Mark where leukocytes are.
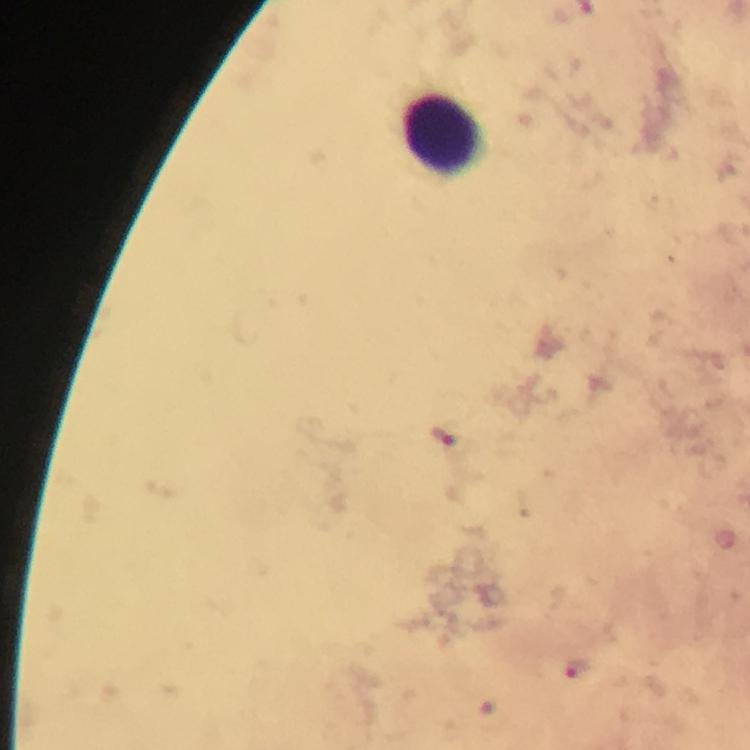
Approximate centers as {x, y} in pixels.
Leukocytes: {440, 136}.

Summary:
  - Plasmodium parasite locations: {443, 435}, {577, 668}
  - Immersion oil: used
  - Cropped from: one field of view
  - Stain: Giemsa
  - Capture: smartphone photograph through a microscope
  - Preparation: thick smear
  - Context: from a diagnostic examination for malaria
  - Magnification: 100x
  - Image size: 750×750 pixels